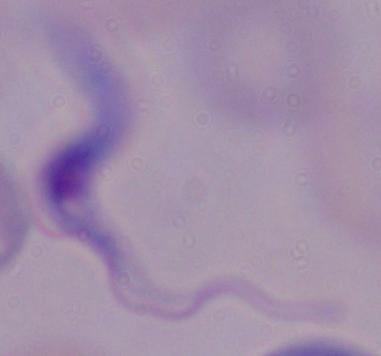 A trypanosome is shown. Captured at 1000x magnification. Micrograph.